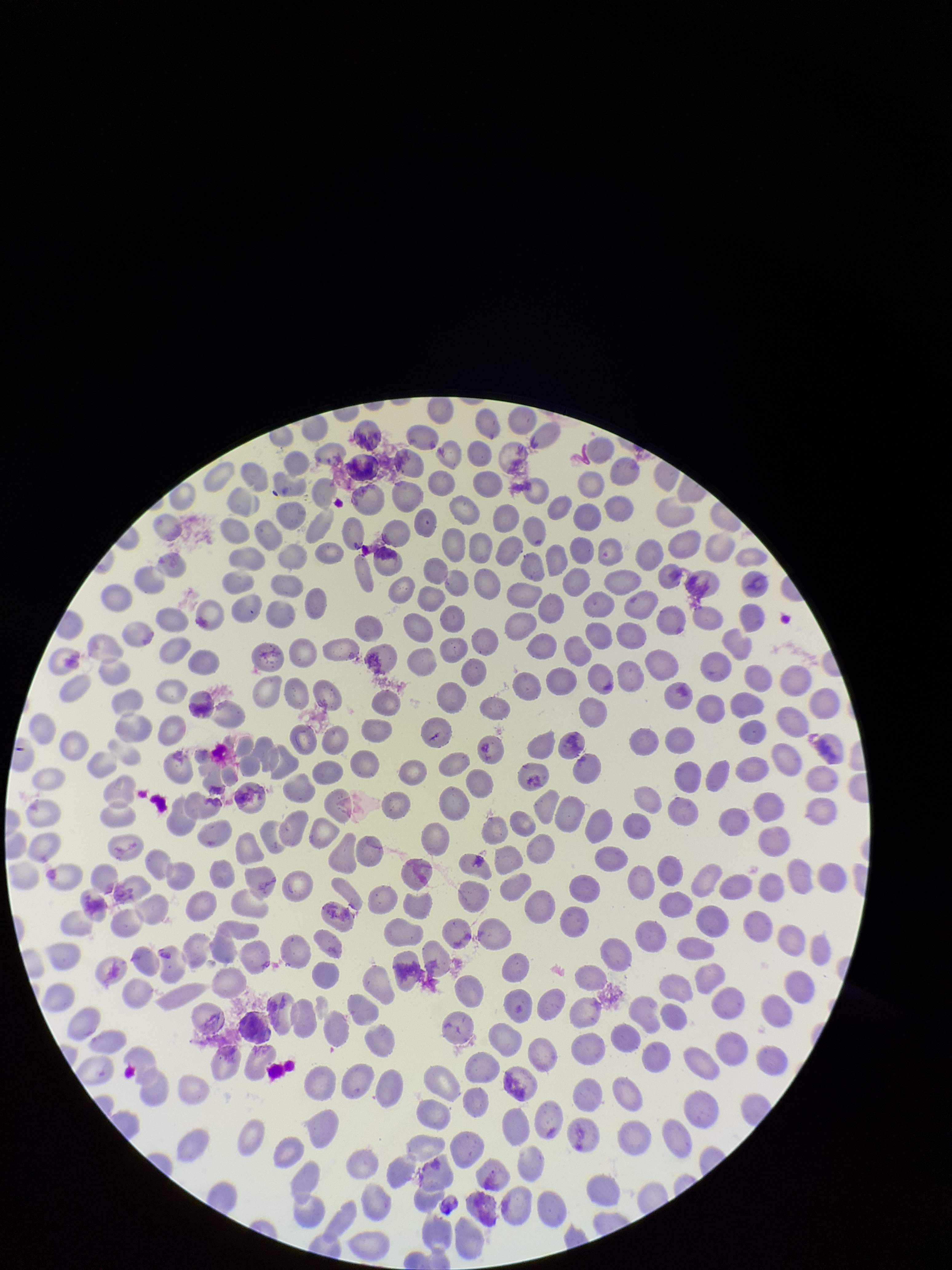

image size = 952×1270 pixels
parasitized red blood cells = none seen
capture = smartphone photograph through the microscope eyepiece
patient malaria status = negative
field of view = single
parasitized red blood cell count = 0
preparation = thin smear
red blood cell count = 333
stain = Giemsa